Describe the morphology of the erythrocytes.
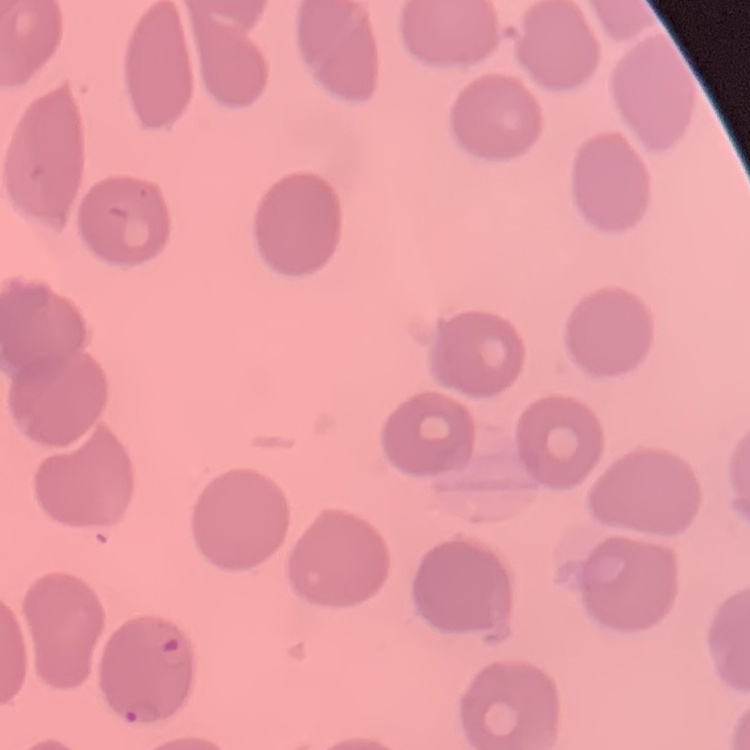
They show no rouleaux formation.

One tile cut from a larger photomicrograph. Thin peripheral smear. Stained with either Field's or Giemsa.